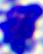

A leukocyte is shown. 400x magnification. Micrograph.